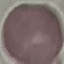

Malaria status: uninfected. Photographed with a smartphone camera at the microscope eyepiece. Cell patch, automatically extracted from a larger field of view and resized to 64 × 64 pixels. Thin blood smear. Giemsa-stained preparation.